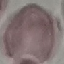
Malaria status: uninfected. Thin blood smear. Photographed with a smartphone camera at the microscope eyepiece. Automatically extracted cell patch, resized to 64 × 64 pixels. Giemsa-stained preparation.